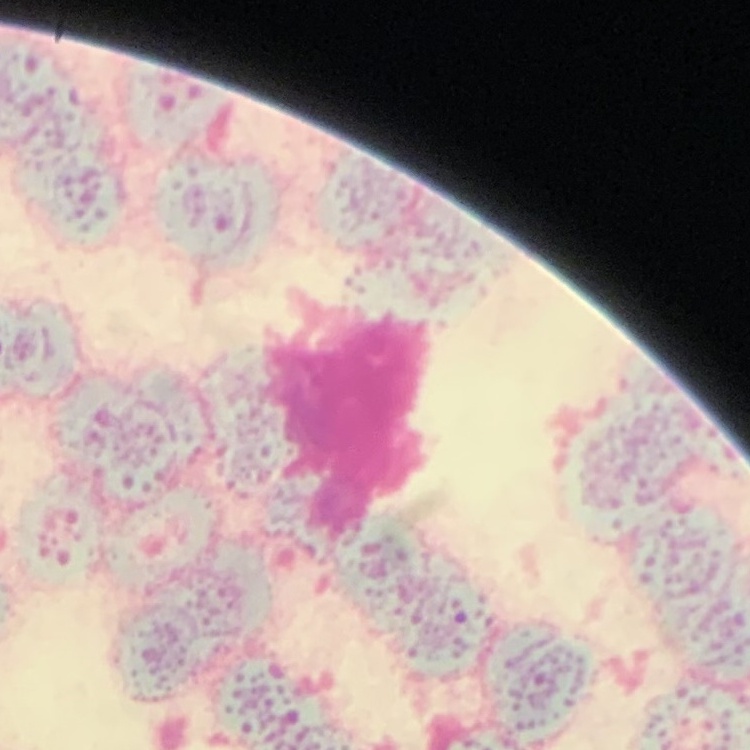
Summary:
  - Red blood cell morphology: rouleaux formation
  - Image type: square crop of a larger photomicrograph
  - Preparation: thin blood film
  - Stain: Field's or Giemsa